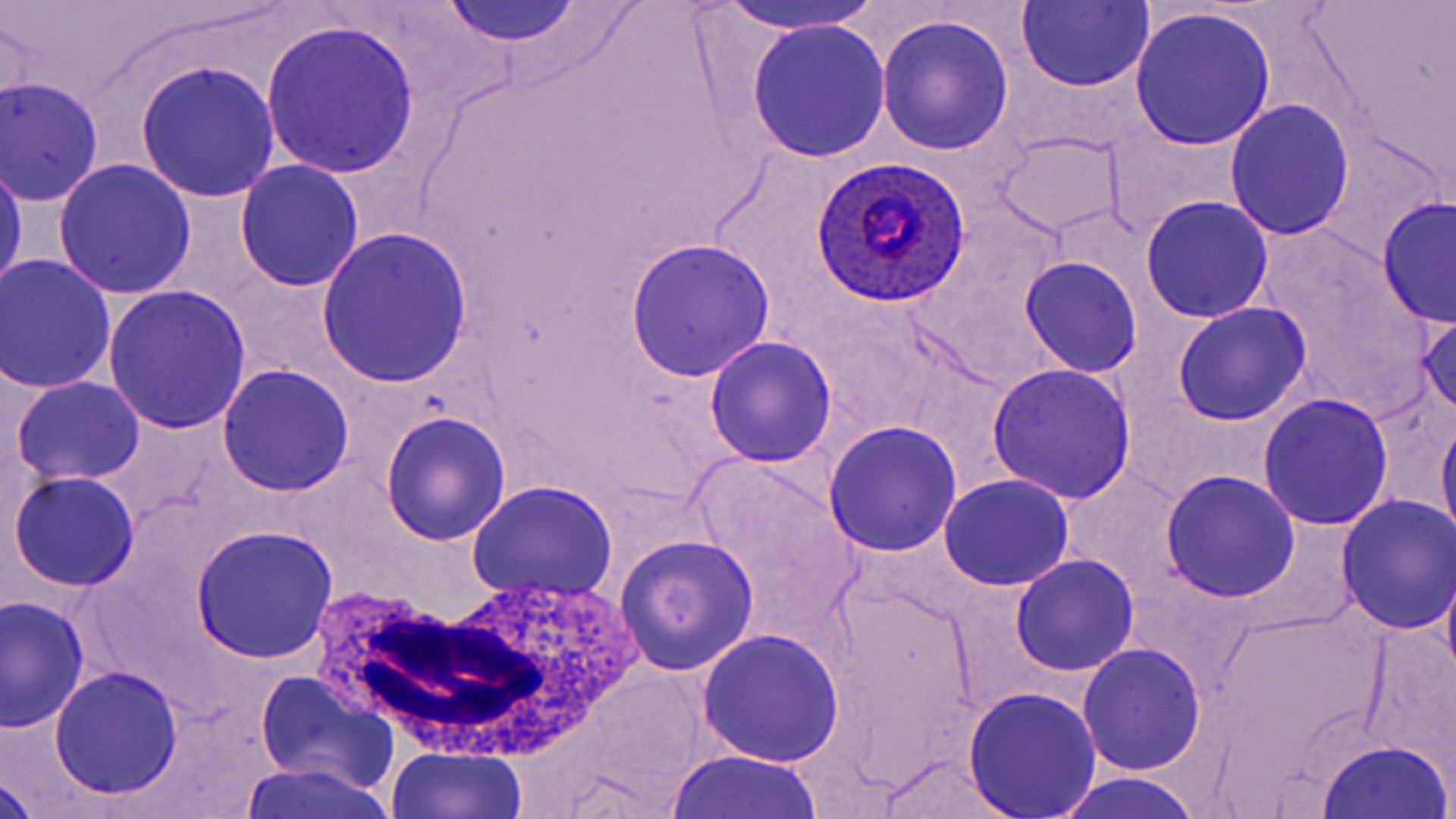

slide-level diagnosis = Plasmodium ovale
field of view = one of a larger specimen
preparation = thin blood smear
image size = 1456×819 pixels
magnification = 1000x
uninfected red blood cell locations = approximate bounding boxes as (x1,y1)-(x2,y2) corner pairs in pixels: (707,0)-(883,37), (1015,1)-(1153,92), (436,3)-(590,48), (1130,8)-(1276,150), (878,16)-(1014,157), (747,19)-(889,161), (260,20)-(420,179), (135,60)-(281,201), (1,76)-(103,207), (1224,100)-(1355,239), (995,131)-(1123,239), (1,153)-(26,297), (53,159)-(196,300), (233,161)-(365,293), (1141,195)-(1274,323), (1376,196)-(1455,328), (315,226)-(475,388), (623,237)-(777,381), (1,255)-(117,395), (1019,255)-(1144,378), (102,285)-(251,435), (1173,302)-(1312,426), (1416,309)-(1456,420), (705,336)-(836,468), (986,362)-(1138,506), (217,366)-(353,498), (11,377)-(146,487), (1256,393)-(1394,530), (1437,409)-(1456,546), (378,411)-(511,546), (825,421)-(961,557), (689,456)-(861,639), (1159,469)-(1300,601), (1060,470)-(1181,589), (9,471)-(140,592), (940,473)-(1075,591), (467,482)-(618,601), (1335,496)-(1454,634), (190,525)-(338,663), (615,533)-(758,675), (1010,555)-(1138,676), (1440,560)-(1456,691), (820,580)-(980,776), (1,596)-(89,732), (696,627)-(845,767), (1359,630)-(1454,785), (1079,642)-(1205,777), (50,666)-(183,801), (254,670)-(399,798), (963,688)-(1102,818), (1317,740)-(1453,818), (385,747)-(528,819), (666,749)-(826,819), (875,753)-(1022,818), (237,761)-(397,819), (1052,771)-(1209,819), (0,774)-(39,819)
stain = May-Grünwald-Giemsa
Plasmodium ovale-infected red blood cell locations = approximate bounding boxes as (x1,y1)-(x2,y2) corner pairs in pixels: (811,157)-(973,309)
white blood cell locations = approximate bounding boxes as (x1,y1)-(x2,y2) corner pairs in pixels: (296,574)-(643,768)
modality = optical microscopy